Locate every Plasmodium falciparum-infected red blood cell.
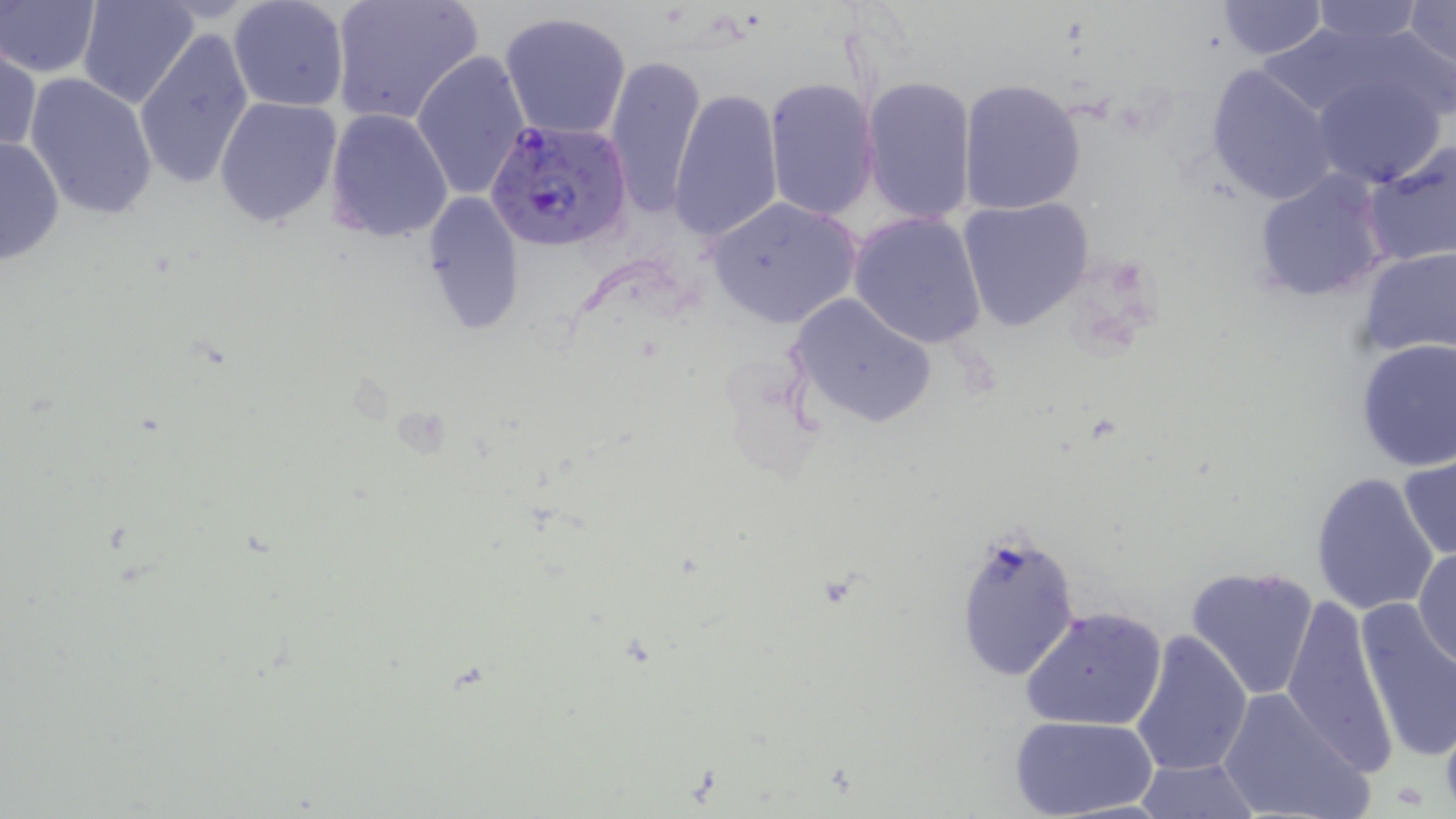

Approximate bounding boxes as (x1,y1)-(x2,y2) corner pairs in pixels.
Plasmodium falciparum-infected red blood cells: (485,117)-(634,252).

slide-level diagnosis = Plasmodium falciparum
preparation = thin blood smear
magnification = 1000x
modality = optical microscopy
stain = May-Grünwald-Giemsa
uninfected red blood cell locations = approximate bounding boxes as (x1,y1)-(x2,y2) corner pairs in pixels: (0,0)-(102,78), (76,0)-(201,109), (328,0)-(484,127), (1214,0)-(1327,59), (1304,0)-(1432,47), (226,1)-(350,113), (1405,1)-(1455,73), (500,9)-(634,141), (1251,21)-(1398,124), (133,27)-(253,193), (0,42)-(41,155), (410,50)-(530,202), (603,51)-(706,219), (1204,63)-(1339,206), (1308,69)-(1450,190), (25,72)-(159,221), (861,74)-(977,225), (765,77)-(881,221), (958,79)-(1088,216), (667,85)-(783,244), (216,94)-(342,229), (326,109)-(454,242), (0,135)-(65,267), (1362,138)-(1456,269), (1251,168)-(1393,304), (423,191)-(525,332), (958,195)-(1098,332), (705,196)-(862,329), (848,211)-(988,348), (1357,248)-(1456,359), (786,294)-(937,430), (1354,338)-(1456,471), (1399,452)-(1456,562), (1310,470)-(1442,616), (952,527)-(1082,684), (1413,545)-(1456,668), (1185,565)-(1320,700), (1282,592)-(1401,774), (1353,597)-(1456,765), (1022,605)-(1167,731), (1129,628)-(1253,779), (1217,688)-(1372,819), (1009,715)-(1157,819), (1131,755)-(1263,818)
platelet locations = approximate bounding boxes as (x1,y1)-(x2,y2) corner pairs in pixels: (1394,780)-(1432,810)
image size = 1456×819 pixels
field of view = single